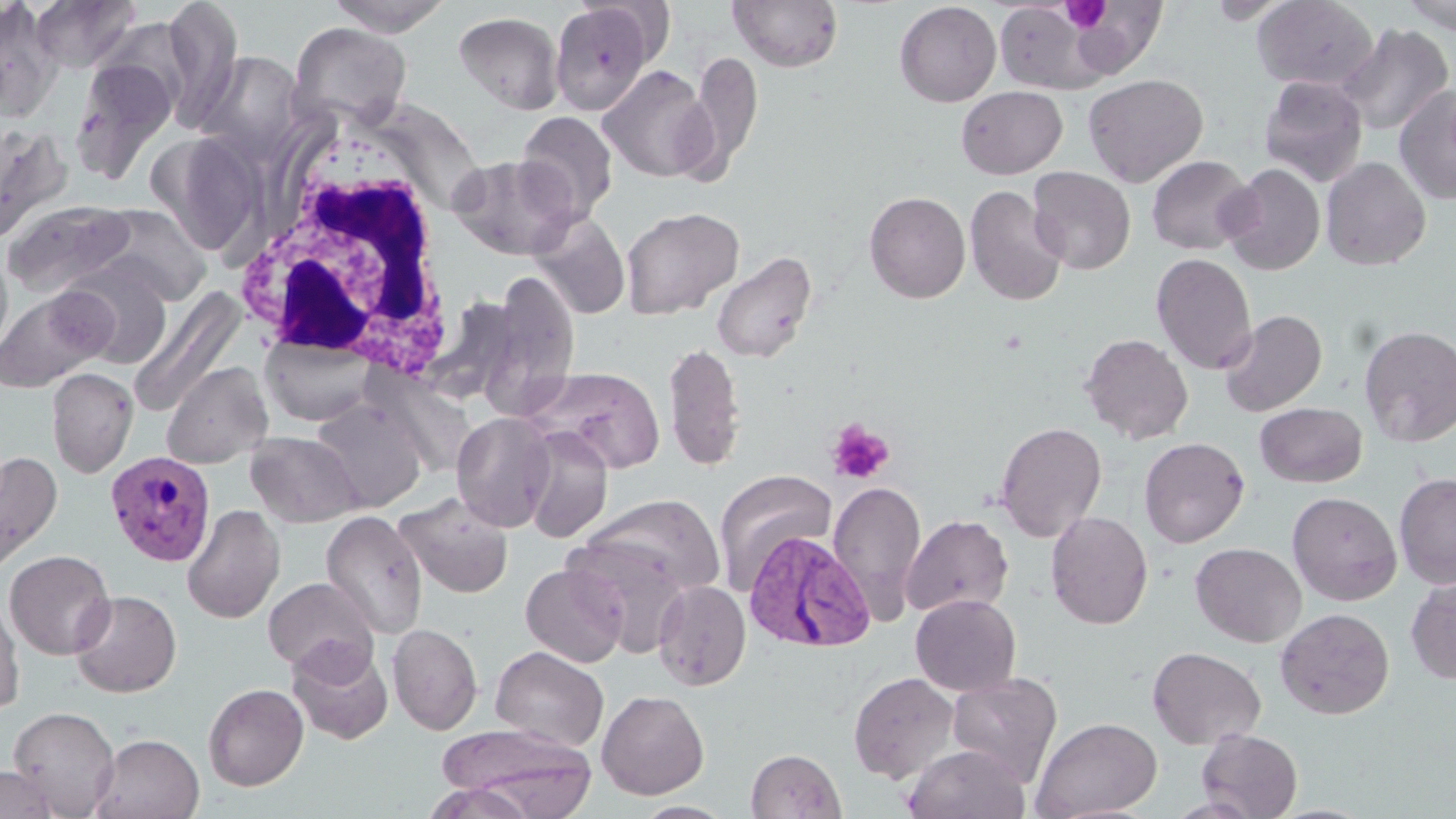

slide-level diagnosis = Plasmodium vivax
preparation = thin blood smear
Plasmodium vivax-infected red blood cell locations = approximate bounding boxes as named x1/y1/x2/y2 corners in pixels: (x1=105, y1=450, x2=217, y2=567), (x1=743, y1=530, x2=875, y2=653)
white blood cell locations = approximate bounding boxes as named x1/y1/x2/y2 corners in pixels: (x1=239, y1=132, x2=461, y2=378)
field of view = single
modality = optical microscopy
stain = May-Grünwald-Giemsa
uninfected red blood cell locations = approximate bounding boxes as named x1/y1/x2/y2 corners in pixels: (x1=30, y1=0, x2=141, y2=73), (x1=161, y1=0, x2=244, y2=125), (x1=325, y1=0, x2=454, y2=36), (x1=729, y1=0, x2=843, y2=73), (x1=1252, y1=0, x2=1379, y2=91), (x1=1401, y1=0, x2=1456, y2=34), (x1=894, y1=1, x2=1001, y2=107), (x1=0, y1=2, x2=62, y2=120), (x1=1069, y1=2, x2=1168, y2=79), (x1=549, y1=3, x2=655, y2=114), (x1=995, y1=4, x2=1107, y2=96), (x1=454, y1=12, x2=564, y2=114), (x1=98, y1=19, x2=197, y2=115), (x1=288, y1=21, x2=412, y2=128), (x1=1335, y1=23, x2=1454, y2=137), (x1=197, y1=51, x2=304, y2=158), (x1=690, y1=51, x2=763, y2=174), (x1=71, y1=56, x2=180, y2=181), (x1=597, y1=64, x2=716, y2=182), (x1=1083, y1=73, x2=1208, y2=187), (x1=1259, y1=75, x2=1368, y2=187), (x1=1394, y1=84, x2=1456, y2=205), (x1=956, y1=85, x2=1067, y2=179), (x1=516, y1=111, x2=618, y2=222), (x1=0, y1=123, x2=70, y2=243), (x1=450, y1=154, x2=580, y2=260), (x1=1146, y1=155, x2=1255, y2=255), (x1=1321, y1=156, x2=1431, y2=270), (x1=1220, y1=163, x2=1326, y2=275), (x1=1028, y1=166, x2=1135, y2=274), (x1=965, y1=185, x2=1068, y2=306), (x1=864, y1=191, x2=970, y2=303), (x1=3, y1=199, x2=136, y2=298), (x1=88, y1=204, x2=211, y2=306), (x1=621, y1=207, x2=744, y2=320), (x1=529, y1=213, x2=630, y2=320), (x1=0, y1=248, x2=14, y2=361), (x1=710, y1=251, x2=818, y2=363), (x1=1151, y1=253, x2=1257, y2=374), (x1=59, y1=262, x2=174, y2=368), (x1=484, y1=273, x2=581, y2=404), (x1=0, y1=287, x2=110, y2=392), (x1=131, y1=288, x2=246, y2=416), (x1=1219, y1=310, x2=1327, y2=416), (x1=1358, y1=324, x2=1456, y2=447), (x1=1080, y1=333, x2=1193, y2=444), (x1=261, y1=334, x2=377, y2=426), (x1=662, y1=341, x2=745, y2=470), (x1=161, y1=361, x2=272, y2=469), (x1=523, y1=366, x2=666, y2=473), (x1=46, y1=367, x2=138, y2=478), (x1=311, y1=398, x2=427, y2=513), (x1=1255, y1=402, x2=1366, y2=487), (x1=451, y1=412, x2=557, y2=532), (x1=994, y1=421, x2=1107, y2=542), (x1=520, y1=427, x2=613, y2=542), (x1=246, y1=431, x2=362, y2=527), (x1=1139, y1=437, x2=1249, y2=547), (x1=0, y1=449, x2=61, y2=579), (x1=713, y1=470, x2=837, y2=593), (x1=1394, y1=472, x2=1456, y2=590), (x1=827, y1=480, x2=926, y2=620), (x1=1287, y1=491, x2=1402, y2=605), (x1=394, y1=492, x2=514, y2=598), (x1=578, y1=493, x2=726, y2=600), (x1=182, y1=504, x2=285, y2=624), (x1=320, y1=510, x2=429, y2=640), (x1=1046, y1=511, x2=1153, y2=629), (x1=900, y1=514, x2=1013, y2=617), (x1=561, y1=536, x2=693, y2=654), (x1=1190, y1=542, x2=1307, y2=647), (x1=4, y1=550, x2=116, y2=660), (x1=520, y1=563, x2=628, y2=667), (x1=1406, y1=575, x2=1456, y2=685), (x1=263, y1=577, x2=379, y2=679), (x1=653, y1=579, x2=752, y2=691), (x1=69, y1=589, x2=182, y2=697), (x1=0, y1=593, x2=24, y2=717), (x1=910, y1=594, x2=1021, y2=696), (x1=1275, y1=608, x2=1394, y2=720), (x1=387, y1=622, x2=483, y2=734), (x1=287, y1=641, x2=394, y2=745), (x1=490, y1=646, x2=609, y2=752), (x1=1147, y1=646, x2=1266, y2=749), (x1=848, y1=672, x2=960, y2=784), (x1=947, y1=672, x2=1062, y2=786), (x1=203, y1=683, x2=309, y2=790), (x1=596, y1=690, x2=709, y2=800), (x1=8, y1=706, x2=120, y2=817), (x1=1031, y1=716, x2=1163, y2=819), (x1=440, y1=725, x2=596, y2=817), (x1=1196, y1=728, x2=1302, y2=818), (x1=90, y1=732, x2=205, y2=819), (x1=903, y1=743, x2=1031, y2=819), (x1=746, y1=748, x2=846, y2=819), (x1=0, y1=765, x2=60, y2=819), (x1=423, y1=781, x2=539, y2=819), (x1=1165, y1=797, x2=1263, y2=818), (x1=631, y1=801, x2=736, y2=819)
magnification = 1000x
image size = 1456×819 pixels
platelet locations = approximate bounding boxes as named x1/y1/x2/y2 corners in pixels: (x1=1062, y1=2, x2=1109, y2=33), (x1=826, y1=419, x2=894, y2=484)